Give the extent of all Plasmodium falciparum-infected red blood cells.
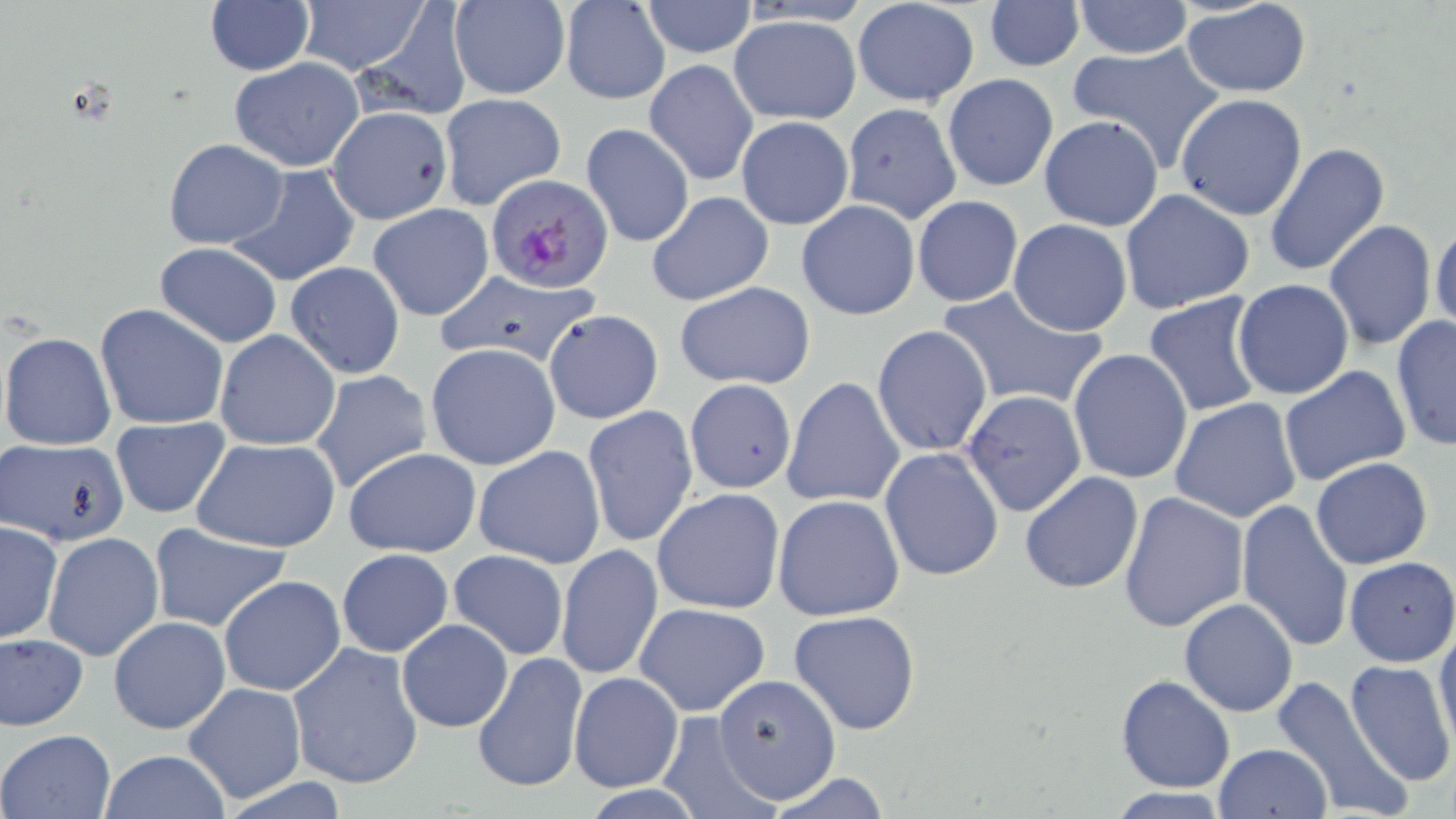

Approximate bounding boxes as named x1/y1/x2/y2 corners in pixels.
Plasmodium falciparum-infected red blood cells: (x1=485, y1=174, x2=615, y2=293).

Summary:
  - Uninfected red blood cell locations: (x1=204, y1=0, x2=315, y2=76), (x1=295, y1=0, x2=429, y2=76), (x1=559, y1=0, x2=672, y2=104), (x1=983, y1=0, x2=1083, y2=72), (x1=638, y1=1, x2=759, y2=58), (x1=850, y1=1, x2=981, y2=107), (x1=1072, y1=1, x2=1194, y2=58), (x1=1180, y1=1, x2=1312, y2=96), (x1=448, y1=2, x2=571, y2=100), (x1=353, y1=5, x2=474, y2=121), (x1=728, y1=14, x2=861, y2=124), (x1=1065, y1=43, x2=1226, y2=172), (x1=229, y1=57, x2=364, y2=171), (x1=644, y1=58, x2=758, y2=187), (x1=942, y1=73, x2=1059, y2=193), (x1=438, y1=92, x2=567, y2=211), (x1=1176, y1=93, x2=1308, y2=221), (x1=841, y1=103, x2=962, y2=224), (x1=327, y1=106, x2=452, y2=225), (x1=736, y1=116, x2=853, y2=230), (x1=1038, y1=116, x2=1164, y2=230), (x1=581, y1=122, x2=694, y2=248), (x1=163, y1=138, x2=288, y2=249), (x1=1264, y1=143, x2=1391, y2=277), (x1=224, y1=162, x2=360, y2=286), (x1=1118, y1=189, x2=1256, y2=316), (x1=646, y1=191, x2=774, y2=307), (x1=912, y1=195, x2=1023, y2=307), (x1=795, y1=200, x2=921, y2=321), (x1=367, y1=203, x2=495, y2=322), (x1=1007, y1=219, x2=1132, y2=336), (x1=1322, y1=220, x2=1437, y2=352), (x1=1430, y1=221, x2=1456, y2=335), (x1=154, y1=242, x2=283, y2=347), (x1=286, y1=261, x2=406, y2=379), (x1=427, y1=271, x2=604, y2=371), (x1=1233, y1=279, x2=1354, y2=399), (x1=675, y1=281, x2=816, y2=389), (x1=936, y1=285, x2=1107, y2=413), (x1=1142, y1=292, x2=1266, y2=419), (x1=94, y1=303, x2=230, y2=430), (x1=543, y1=308, x2=664, y2=424), (x1=1390, y1=312, x2=1456, y2=453), (x1=871, y1=325, x2=993, y2=457), (x1=215, y1=329, x2=341, y2=453), (x1=0, y1=331, x2=117, y2=452), (x1=425, y1=343, x2=561, y2=470), (x1=1067, y1=348, x2=1193, y2=485), (x1=1279, y1=365, x2=1410, y2=485), (x1=309, y1=369, x2=433, y2=495), (x1=782, y1=376, x2=905, y2=508), (x1=684, y1=380, x2=797, y2=493), (x1=960, y1=391, x2=1086, y2=518), (x1=1170, y1=397, x2=1302, y2=523), (x1=582, y1=406, x2=699, y2=548), (x1=109, y1=415, x2=233, y2=522), (x1=191, y1=437, x2=341, y2=552), (x1=3, y1=439, x2=132, y2=546), (x1=474, y1=445, x2=606, y2=568), (x1=878, y1=446, x2=1004, y2=582), (x1=343, y1=448, x2=481, y2=558), (x1=1310, y1=457, x2=1433, y2=570), (x1=1019, y1=472, x2=1144, y2=593), (x1=652, y1=487, x2=785, y2=614), (x1=1118, y1=491, x2=1248, y2=633), (x1=772, y1=495, x2=903, y2=620), (x1=1236, y1=499, x2=1354, y2=653), (x1=1, y1=521, x2=62, y2=644), (x1=149, y1=523, x2=291, y2=632), (x1=44, y1=532, x2=164, y2=661), (x1=555, y1=543, x2=664, y2=684), (x1=337, y1=548, x2=453, y2=656), (x1=448, y1=549, x2=570, y2=660), (x1=1345, y1=557, x2=1456, y2=666), (x1=217, y1=575, x2=347, y2=697), (x1=1180, y1=598, x2=1298, y2=717), (x1=633, y1=602, x2=770, y2=716), (x1=789, y1=609, x2=921, y2=736), (x1=107, y1=615, x2=232, y2=736), (x1=395, y1=618, x2=514, y2=733), (x1=1434, y1=624, x2=1456, y2=752), (x1=1, y1=635, x2=88, y2=730), (x1=286, y1=640, x2=424, y2=790), (x1=472, y1=651, x2=586, y2=794), (x1=1344, y1=662, x2=1455, y2=787), (x1=569, y1=671, x2=683, y2=792), (x1=710, y1=673, x2=841, y2=804), (x1=1115, y1=675, x2=1235, y2=792), (x1=1272, y1=676, x2=1410, y2=818), (x1=182, y1=681, x2=308, y2=803), (x1=655, y1=710, x2=772, y2=817), (x1=1, y1=729, x2=114, y2=818), (x1=1211, y1=743, x2=1332, y2=818), (x1=99, y1=749, x2=232, y2=819), (x1=761, y1=770, x2=893, y2=817), (x1=1102, y1=787, x2=1234, y2=817)
  - Slide-level diagnosis: Plasmodium falciparum
  - Image size: 1456×819 pixels
  - Field of view: one of a larger specimen
  - Stain: May-Grünwald-Giemsa
  - Modality: light microscopy
  - Preparation: thin blood film
  - Magnification: 1000x